Locate and identify every blood parasite.
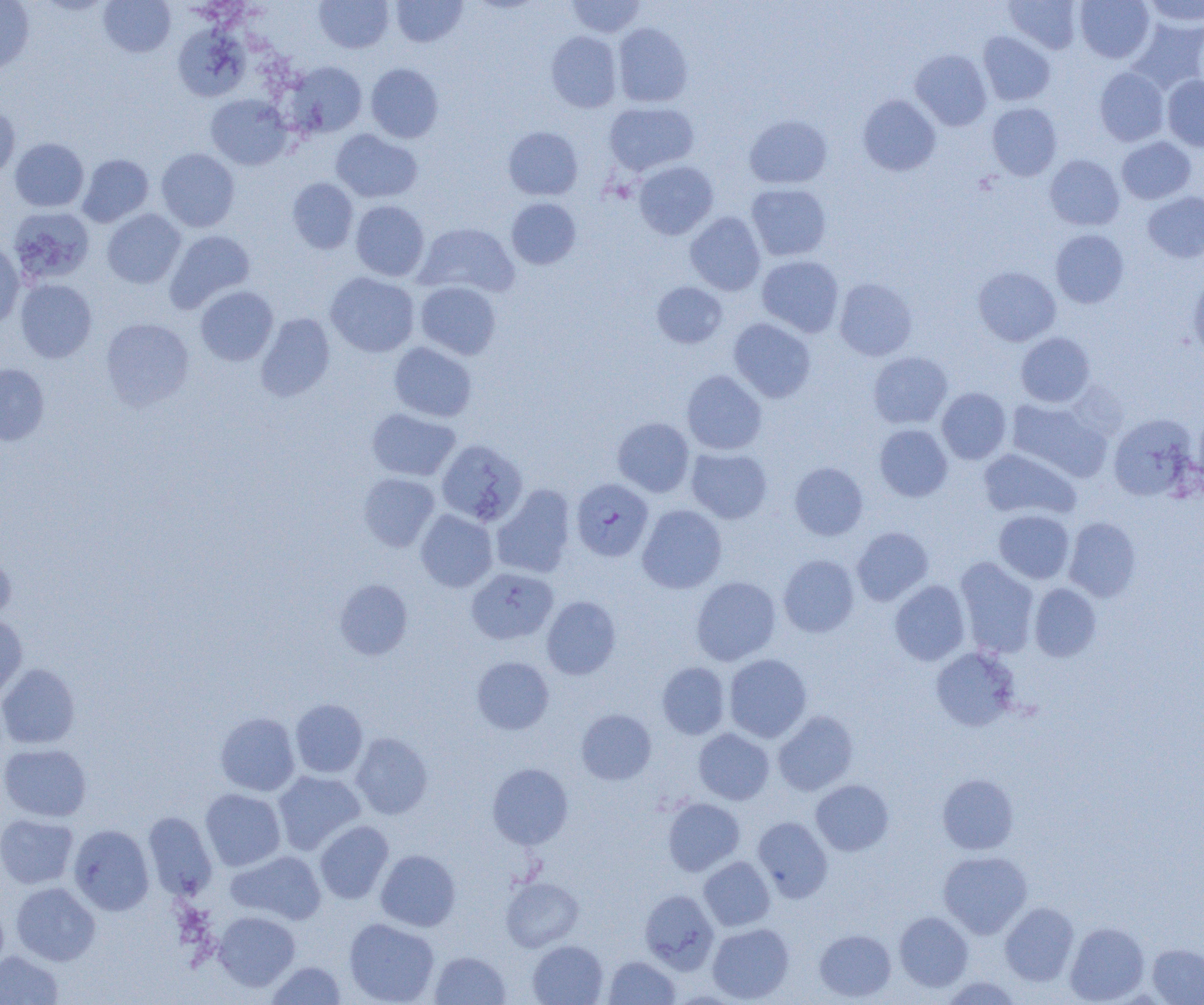

Approximate bounding boxes as named x1/y1/x2/y2 corners in pixels.
Plasmodium falciparum-infected red blood cells: (x1=571, y1=478, x2=653, y2=562).
No Plasmodium ovale, Plasmodium malariae, Plasmodium vivax, Babesia divergens, or Trypanosoma brucei observed.

Uninfected red blood cell locations: (x1=99, y1=0, x2=175, y2=58), (x1=391, y1=0, x2=467, y2=47), (x1=565, y1=0, x2=647, y2=38), (x1=1004, y1=0, x2=1081, y2=53), (x1=1075, y1=0, x2=1154, y2=63), (x1=1141, y1=0, x2=1203, y2=28), (x1=0, y1=1, x2=34, y2=74), (x1=314, y1=1, x2=393, y2=53), (x1=1127, y1=17, x2=1204, y2=95), (x1=613, y1=22, x2=693, y2=107), (x1=173, y1=23, x2=249, y2=102), (x1=546, y1=31, x2=622, y2=112), (x1=978, y1=31, x2=1055, y2=105), (x1=911, y1=50, x2=992, y2=130), (x1=286, y1=61, x2=367, y2=138), (x1=366, y1=63, x2=444, y2=143), (x1=1094, y1=67, x2=1169, y2=146), (x1=1162, y1=75, x2=1204, y2=152), (x1=206, y1=94, x2=292, y2=170), (x1=858, y1=94, x2=941, y2=176), (x1=604, y1=101, x2=698, y2=175), (x1=0, y1=102, x2=20, y2=179), (x1=987, y1=102, x2=1062, y2=181), (x1=744, y1=115, x2=832, y2=188), (x1=503, y1=126, x2=583, y2=200), (x1=330, y1=129, x2=422, y2=203), (x1=1116, y1=136, x2=1195, y2=205), (x1=10, y1=138, x2=89, y2=212), (x1=156, y1=148, x2=240, y2=232), (x1=78, y1=154, x2=154, y2=227), (x1=1045, y1=154, x2=1124, y2=230), (x1=633, y1=161, x2=718, y2=240), (x1=287, y1=178, x2=358, y2=254), (x1=746, y1=183, x2=832, y2=261), (x1=1143, y1=191, x2=1204, y2=263), (x1=506, y1=198, x2=581, y2=269), (x1=350, y1=200, x2=429, y2=281), (x1=8, y1=206, x2=95, y2=285), (x1=102, y1=209, x2=185, y2=288), (x1=685, y1=212, x2=765, y2=295), (x1=415, y1=223, x2=519, y2=298), (x1=165, y1=229, x2=255, y2=312), (x1=1050, y1=229, x2=1129, y2=308), (x1=0, y1=241, x2=25, y2=327), (x1=757, y1=255, x2=844, y2=337), (x1=973, y1=266, x2=1061, y2=346), (x1=325, y1=272, x2=419, y2=357), (x1=1188, y1=273, x2=1204, y2=361), (x1=834, y1=278, x2=917, y2=360), (x1=15, y1=279, x2=97, y2=363), (x1=652, y1=281, x2=727, y2=348), (x1=415, y1=282, x2=501, y2=359), (x1=195, y1=285, x2=278, y2=366), (x1=256, y1=313, x2=335, y2=401), (x1=101, y1=317, x2=194, y2=410), (x1=728, y1=318, x2=816, y2=402), (x1=1016, y1=332, x2=1095, y2=407), (x1=389, y1=342, x2=477, y2=422), (x1=868, y1=352, x2=953, y2=429), (x1=0, y1=363, x2=50, y2=446), (x1=682, y1=370, x2=767, y2=455), (x1=937, y1=388, x2=1011, y2=464), (x1=1006, y1=398, x2=1110, y2=482), (x1=367, y1=408, x2=460, y2=481), (x1=1108, y1=414, x2=1198, y2=501), (x1=613, y1=417, x2=694, y2=497), (x1=875, y1=424, x2=952, y2=501), (x1=436, y1=438, x2=527, y2=526), (x1=686, y1=447, x2=772, y2=523), (x1=978, y1=448, x2=1080, y2=521), (x1=790, y1=462, x2=868, y2=540), (x1=358, y1=473, x2=439, y2=551), (x1=491, y1=485, x2=576, y2=579), (x1=637, y1=504, x2=726, y2=593), (x1=416, y1=509, x2=497, y2=592), (x1=994, y1=509, x2=1075, y2=583), (x1=1064, y1=517, x2=1141, y2=602), (x1=852, y1=527, x2=933, y2=605), (x1=0, y1=549, x2=16, y2=626), (x1=778, y1=554, x2=860, y2=637), (x1=955, y1=557, x2=1039, y2=657), (x1=466, y1=567, x2=558, y2=644), (x1=691, y1=576, x2=781, y2=665), (x1=334, y1=579, x2=412, y2=660), (x1=890, y1=580, x2=970, y2=666), (x1=1029, y1=583, x2=1102, y2=661), (x1=542, y1=596, x2=621, y2=679), (x1=0, y1=615, x2=28, y2=702), (x1=931, y1=646, x2=1020, y2=731), (x1=724, y1=654, x2=811, y2=742), (x1=472, y1=656, x2=554, y2=734), (x1=657, y1=662, x2=730, y2=739), (x1=0, y1=663, x2=81, y2=748), (x1=290, y1=699, x2=367, y2=778), (x1=576, y1=709, x2=656, y2=785), (x1=773, y1=710, x2=858, y2=796), (x1=215, y1=712, x2=300, y2=796), (x1=693, y1=728, x2=774, y2=804), (x1=351, y1=732, x2=432, y2=819), (x1=0, y1=743, x2=92, y2=821), (x1=487, y1=763, x2=573, y2=849), (x1=273, y1=770, x2=365, y2=855), (x1=937, y1=773, x2=1018, y2=854), (x1=811, y1=780, x2=894, y2=856), (x1=200, y1=788, x2=286, y2=871), (x1=662, y1=797, x2=745, y2=876), (x1=143, y1=811, x2=217, y2=900), (x1=0, y1=814, x2=78, y2=889), (x1=752, y1=816, x2=832, y2=902), (x1=314, y1=821, x2=394, y2=903), (x1=68, y1=825, x2=154, y2=915), (x1=376, y1=849, x2=460, y2=931), (x1=226, y1=850, x2=326, y2=925), (x1=939, y1=851, x2=1032, y2=938), (x1=699, y1=857, x2=775, y2=930), (x1=501, y1=877, x2=583, y2=951), (x1=10, y1=882, x2=100, y2=966), (x1=640, y1=890, x2=718, y2=973), (x1=0, y1=898, x2=9, y2=976), (x1=1000, y1=902, x2=1079, y2=985), (x1=213, y1=911, x2=300, y2=991), (x1=894, y1=911, x2=973, y2=992), (x1=344, y1=917, x2=439, y2=1005), (x1=1065, y1=922, x2=1149, y2=1004), (x1=708, y1=923, x2=794, y2=1003), (x1=814, y1=929, x2=896, y2=1001), (x1=528, y1=940, x2=608, y2=1005), (x1=1147, y1=944, x2=1204, y2=1004), (x1=0, y1=950, x2=63, y2=1005), (x1=430, y1=951, x2=511, y2=1004), (x1=603, y1=956, x2=680, y2=1004), (x1=266, y1=960, x2=346, y2=1004), (x1=938, y1=976, x2=1024, y2=1005). Slide-level diagnosis: Plasmodium falciparum. Single field of view. Thin blood smear. Image is 1204×1005 pixels. Captured at 1000x magnification. Light microscopy.